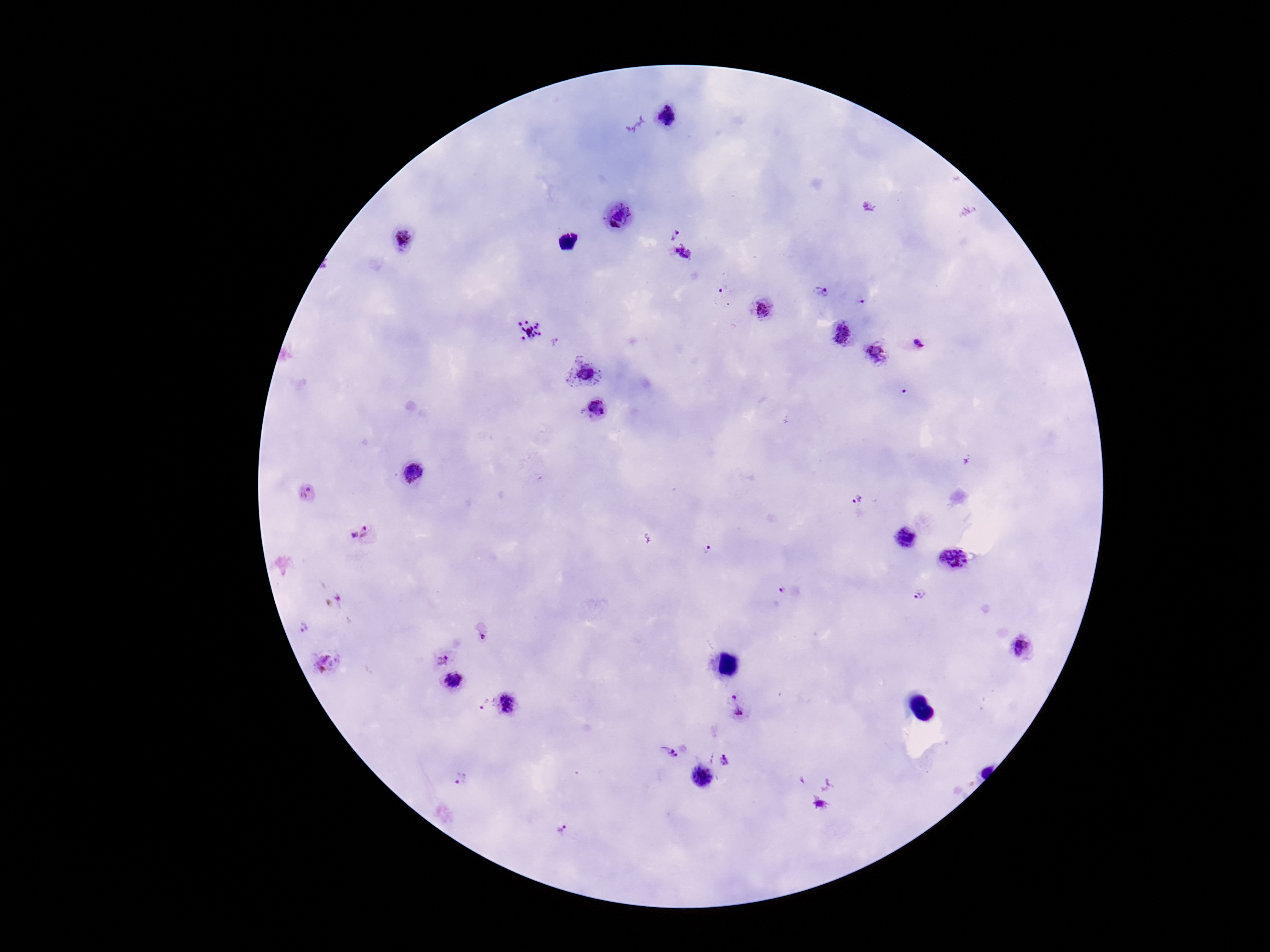
capture = smartphone camera through the microscope eyepiece
patient malaria status = positive
stain = Giemsa
Plasmodium parasite locations = approximate centers as {x, y} in pixels: {666, 116}, {618, 217}, {674, 231}, {403, 240}, {683, 254}, {820, 291}, {723, 292}, {860, 302}, {763, 308}, {530, 332}, {841, 334}, {915, 343}, {876, 354}, {583, 370}, {597, 411}, {413, 473}, {307, 493}, {859, 502}, {352, 536}, {369, 536}, {905, 539}, {708, 551}, {955, 558}, {781, 591}, {916, 595}, {303, 628}, {1025, 646}, {443, 658}, {326, 662}, {453, 681}, {506, 704}, {481, 706}, {738, 707}, {668, 752}, {727, 762}, {702, 778}, {458, 779}, {818, 804}, {562, 829}
magnification = 100x
image size = 1270×952 pixels
field of view = single
preparation = thick peripheral-blood smear